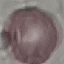

Summary:
  - Malaria status: uninfected
  - Preparation: thin blood film
  - Image type: cell patch, automatically extracted from a larger field of view and resized to 64 × 64 pixels
  - Stain: Giemsa
  - Capture: smartphone through the microscope eyepiece